Name the parasite shown.
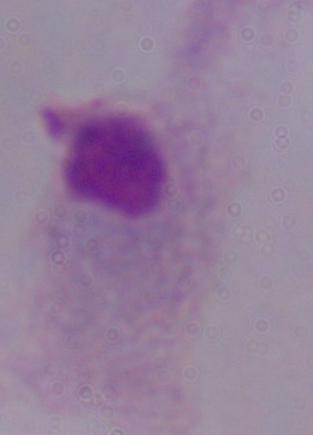
A trichomonad.

Micrograph. Captured at 1000x magnification.